Comment on the morphology of the red blood cells.
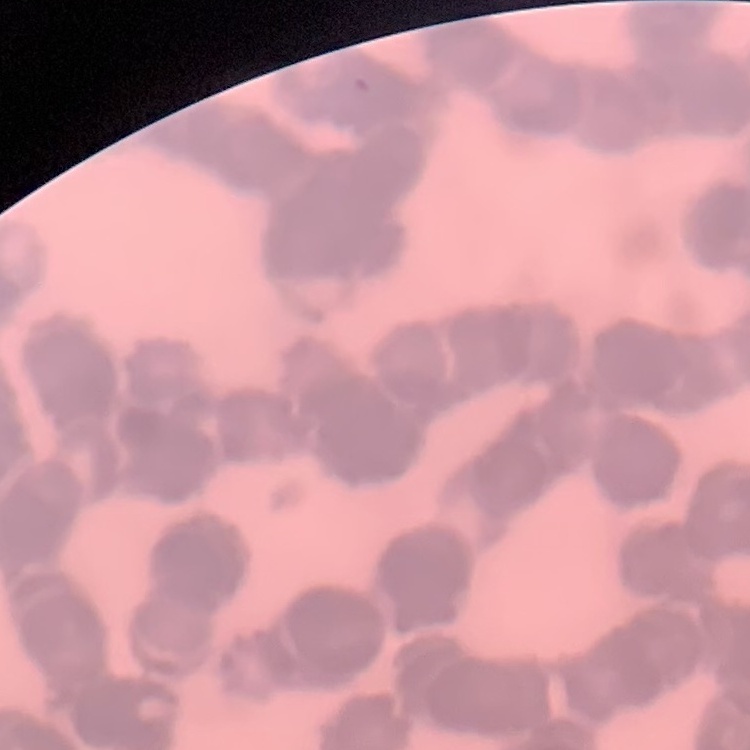
Rouleaux formation.

preparation: thin blood film
stain: Field's or Giemsa
image_type: square crop of a larger photomicrograph